Name the parasite shown.
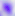

This is Toxoplasma gondii.

modality = micrograph
magnification = 400x